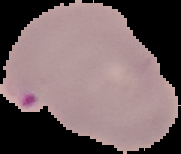
Result: Plasmodium parasites detected. Cell region segmented out of the field of view; the surrounding area is masked to black. From a thin blood film. Image is 181×154 pixels.